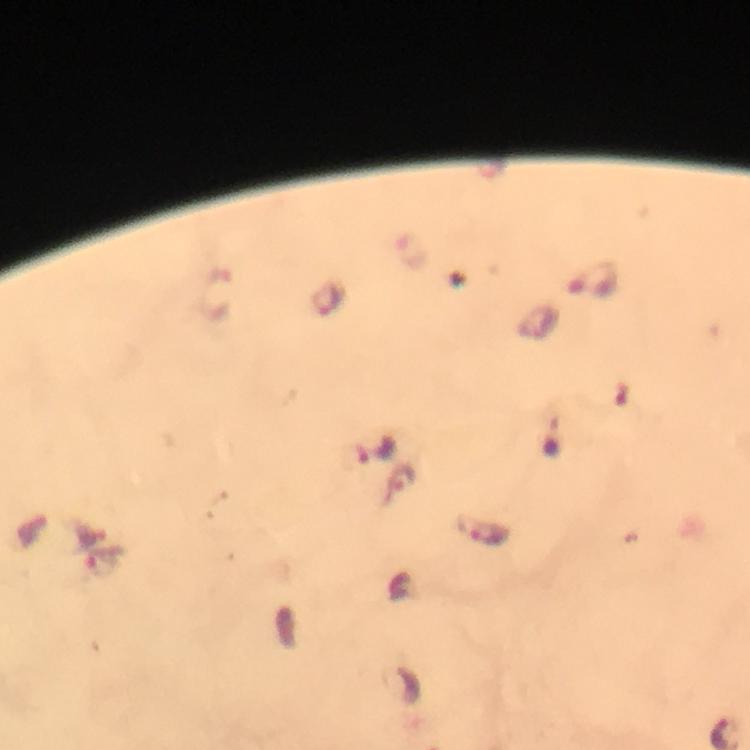

Approximate centers as (x, y) in pixels.
Summary:
  - Malaria parasite locations: (413, 252), (592, 278), (215, 293), (327, 299), (377, 448), (400, 480), (482, 530)
  - Immersion oil: applied
  - Preparation: thick blood film
  - Magnification: 100x
  - Cropped from: one field of view
  - Context: from a malaria diagnostic workup
  - Stain: Giemsa
  - Image size: 750×750 pixels
  - Capture: smartphone camera through the microscope